Outline each blood parasite and name the species.
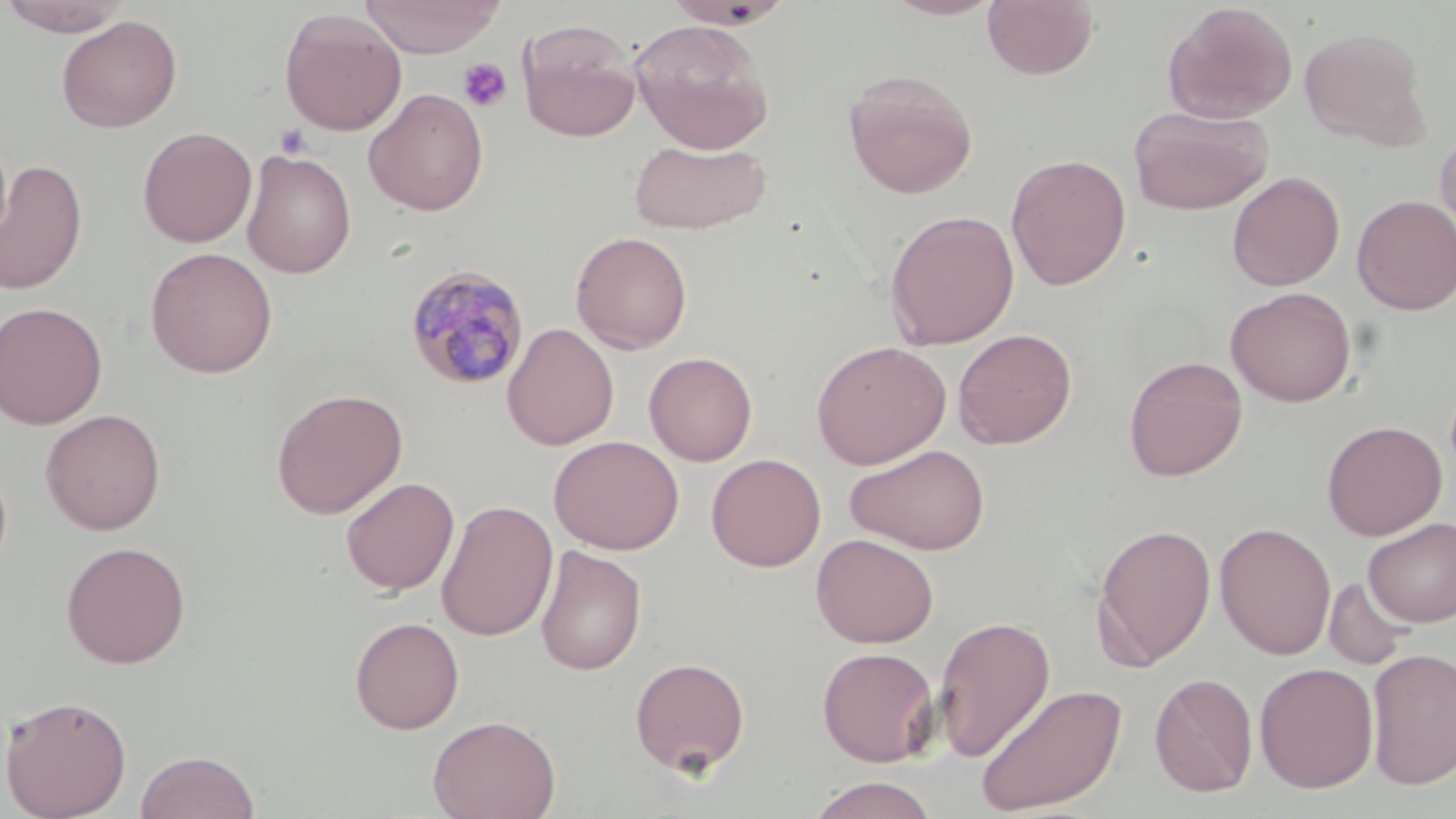

Approximate bounding boxes as (x1, y1, x2, y2) in pixels.
Plasmodium malariae-infected red blood cells: (403, 263, 531, 391).
No Plasmodium falciparum, Plasmodium ovale, Plasmodium vivax, Babesia divergens, or Trypanosoma brucei observed.

Summary:
  - Uninfected red blood cell locations: (359, 0, 506, 58), (883, 0, 1006, 20), (983, 0, 1099, 81), (0, 1, 133, 36), (664, 1, 793, 29), (1162, 1, 1298, 124), (279, 8, 407, 136), (56, 15, 182, 133), (519, 20, 642, 142), (629, 20, 775, 154), (1299, 26, 1430, 149), (843, 69, 978, 198), (363, 88, 489, 216), (1129, 106, 1273, 216), (137, 126, 257, 248), (1435, 130, 1456, 248), (627, 138, 772, 235), (241, 149, 357, 277), (1006, 153, 1131, 290), (1, 159, 88, 295), (1227, 171, 1345, 291), (1352, 194, 1456, 315), (883, 209, 1020, 349), (570, 231, 693, 354), (145, 246, 278, 378), (1225, 286, 1356, 407), (0, 301, 108, 429), (501, 323, 619, 450), (952, 328, 1077, 449), (811, 340, 951, 469), (644, 351, 758, 466), (1123, 355, 1248, 481), (270, 388, 408, 519), (40, 408, 166, 535), (1322, 420, 1447, 540), (548, 435, 685, 555), (844, 443, 991, 555), (706, 453, 827, 571), (340, 476, 459, 596), (436, 499, 558, 642), (1363, 518, 1456, 626), (1091, 521, 1217, 670), (1215, 521, 1336, 660), (811, 534, 939, 648), (60, 541, 191, 669), (535, 545, 647, 675), (1323, 577, 1414, 671), (932, 614, 1055, 764), (349, 616, 464, 734), (816, 646, 940, 767), (1366, 647, 1456, 790), (629, 656, 750, 777), (1253, 662, 1379, 794), (1149, 672, 1259, 797), (975, 682, 1128, 816), (1, 694, 132, 818), (427, 714, 561, 819), (135, 750, 260, 819), (808, 775, 937, 819)
  - Platelet locations: (457, 57, 512, 113), (273, 124, 312, 159)
  - Slide-level diagnosis: Plasmodium malariae
  - Magnification: 1000x
  - Image size: 1456×819 pixels
  - Modality: light microscopy
  - Field of view: single
  - Stain: May-Grünwald-Giemsa
  - Preparation: thin blood smear